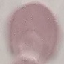
malaria status = uninfected
image type = automatically extracted cell patch, resized to 64 × 64 pixels
stain = Giemsa
capture = smartphone camera at the microscope eyepiece
preparation = thin smear